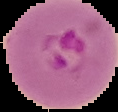
Malaria status: parasitized. From a thin blood film. Image is 118×112 pixels. Cell region segmented out of the field of view; the surrounding area is masked to black.